Mark where cells are.
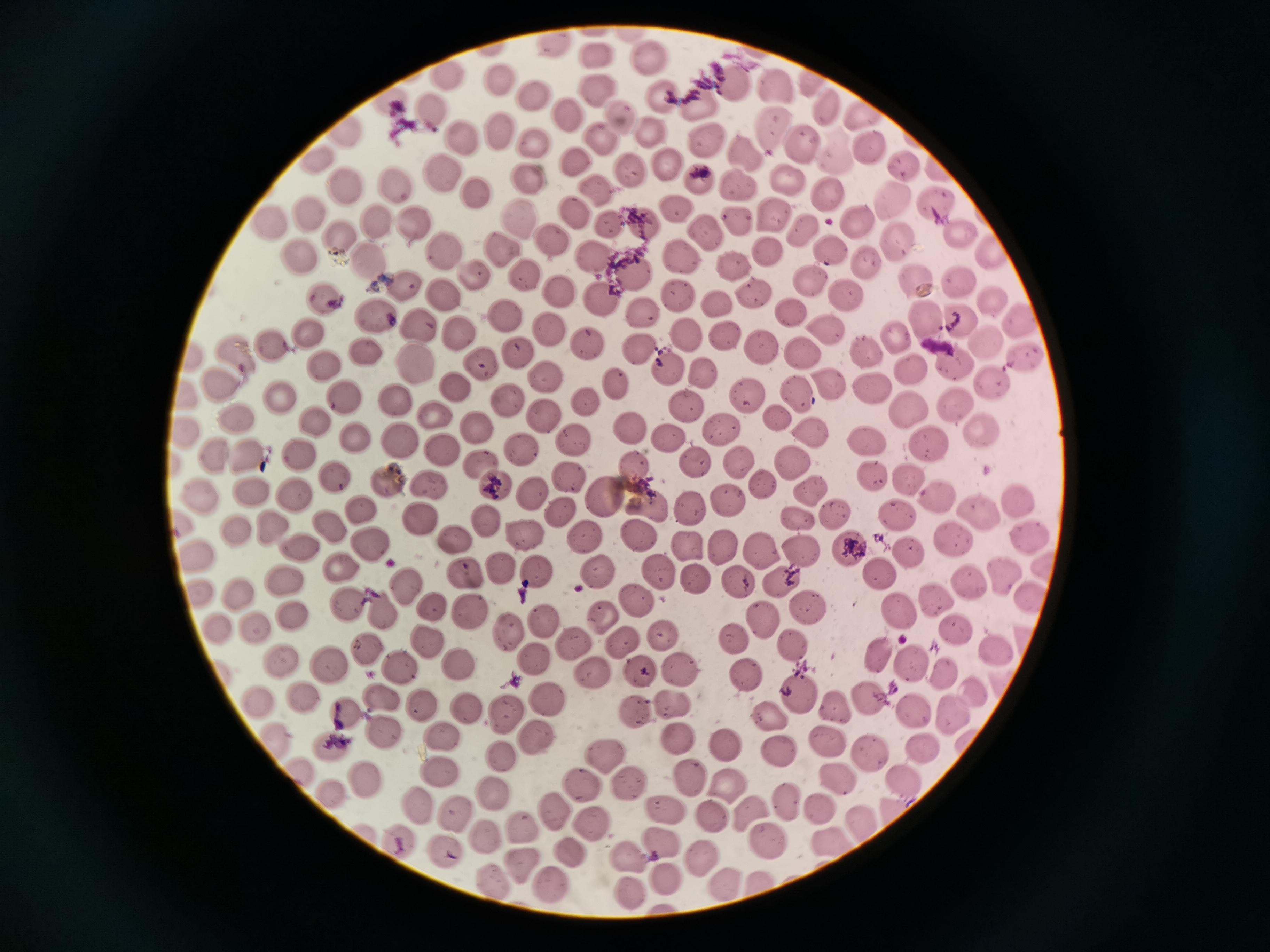
Approximate centers as [x, y] in pixels.
Cells (subset; some too small to resolve): [551, 45], [597, 54], [652, 57], [445, 73], [501, 78], [812, 80], [732, 83], [597, 89], [534, 95], [659, 96], [697, 101], [388, 102], [825, 104], [430, 109], [568, 113], [621, 115], [865, 115], [773, 127], [499, 129], [648, 130], [347, 134], [460, 137], [604, 137], [704, 138], [532, 139], [870, 144], [804, 146], [748, 150], [835, 153], [316, 159], [579, 164], [670, 165], [905, 166], [938, 166], [631, 169], [444, 173], [696, 177], [789, 179], [532, 180], [738, 182], [344, 185], [395, 185], [473, 187], [593, 187], [827, 193], [894, 198], [938, 203], [676, 207], [574, 212], [774, 212], [305, 213], [515, 215], [735, 217], [376, 220], [271, 222], [414, 222], [608, 222], [644, 222], [856, 223], [706, 228], [800, 231], [958, 231], [338, 234], [899, 241], [555, 244], [829, 249], [496, 250], [441, 251], [768, 251], [992, 252], [682, 254], [298, 257], [594, 257], [863, 261], [365, 262], [734, 265], [637, 272], [472, 274], [524, 274], [916, 280], [812, 281], [405, 284], [962, 284], [562, 289], [849, 293], [759, 295], [679, 296], [607, 297], [442, 299], [991, 300], [324, 301], [718, 303], [641, 310], [795, 311], [376, 315], [505, 317], [927, 321], [418, 322], [1021, 322], [963, 324], [552, 330], [827, 330], [310, 331], [458, 335], [730, 337], [981, 338], [687, 339], [276, 340], [890, 341], [588, 344], [762, 344], [236, 349], [800, 349], [363, 350], [639, 351], [518, 354], [193, 355], [865, 355], [414, 361], [1021, 361], [325, 365], [478, 365], [957, 367], [671, 368], [906, 370], [705, 373], [544, 375], [219, 381], [826, 381], [995, 381], [612, 384], [455, 387], [873, 387], [794, 391], [747, 394], [280, 396], [342, 396], [187, 397], [395, 403], [589, 403], [509, 404], [688, 404], [954, 407], [911, 409], [232, 414], [545, 414], [774, 414], [436, 415], [315, 422], [631, 427], [182, 429], [721, 429], [976, 430], [476, 432], [811, 432], [668, 438], [354, 439], [575, 440], [864, 440], [397, 442], [929, 446], [523, 448], [245, 450], [442, 450], [295, 454], [213, 455], [740, 458], [695, 461], [478, 462], [798, 463], [633, 468], [334, 476], [566, 476], [875, 476], [912, 479], [385, 480], [492, 482], [430, 483], [767, 485], [815, 486], [249, 487], [195, 492], [296, 492], [531, 492], [605, 496], [935, 497], [648, 499], [728, 500], [1019, 501], [689, 507], [979, 510], [363, 512], [561, 513], [837, 513], [895, 516], [417, 519], [179, 520], [483, 521], [800, 523], [272, 527], [332, 528], [236, 529], [640, 533], [1032, 535], [522, 536], [954, 536], [585, 538], [455, 541], [369, 546], [847, 546], [719, 547], [761, 547], [803, 547], [297, 548], [688, 551], [198, 553], [908, 553], [1042, 562], [342, 568], [504, 570], [597, 571], [661, 571], [538, 574], [884, 574], [463, 575], [1001, 575], [695, 576], [788, 576], [282, 579], [968, 581], [735, 582], [405, 584], [198, 592], [237, 593], [1033, 593], [939, 598], [640, 602], [814, 604], [348, 605], [433, 606], [387, 612], [902, 613], [291, 615], [475, 615], [605, 616], [766, 620], [215, 624], [548, 625], [254, 626], [508, 630], [955, 630], [660, 636], [425, 638], [737, 639], [625, 641], [798, 644], [574, 646], [997, 647], [369, 648], [531, 656], [883, 657], [276, 658], [912, 664], [459, 665], [331, 666], [643, 669], [402, 670], [681, 672], [943, 672], [594, 675], [747, 677], [973, 692], [797, 694], [257, 698], [304, 699], [870, 699], [546, 700], [384, 703], [671, 704], [425, 708], [470, 709], [837, 709], [347, 712], [636, 712], [953, 712], [915, 713], [504, 714], [769, 715], [381, 730], [443, 732], [683, 735], [536, 739], [831, 741], [278, 743], [728, 744], [329, 746], [919, 746], [781, 753], [603, 756], [868, 757], [501, 758], [302, 771], [439, 772], [691, 775], [840, 777], [366, 780], [903, 782], [625, 783], [581, 786], [728, 786], [329, 795], [494, 796], [788, 800], [413, 804], [892, 804], [450, 808], [552, 810], [663, 810], [820, 811], [751, 812], [714, 815], [596, 822], [859, 823], [519, 827], [485, 837], [398, 839], [768, 839], [660, 840], [825, 840], [445, 851], [566, 851], [695, 853], [631, 858], [522, 864], [666, 877], [493, 881], [755, 882], [551, 883], [720, 884], [628, 890].

image size = 1270×952 pixels
stain = Giemsa
preparation = thin smear
field of view = single
capture = smartphone through the microscope eyepiece